Name the blood parasite species.
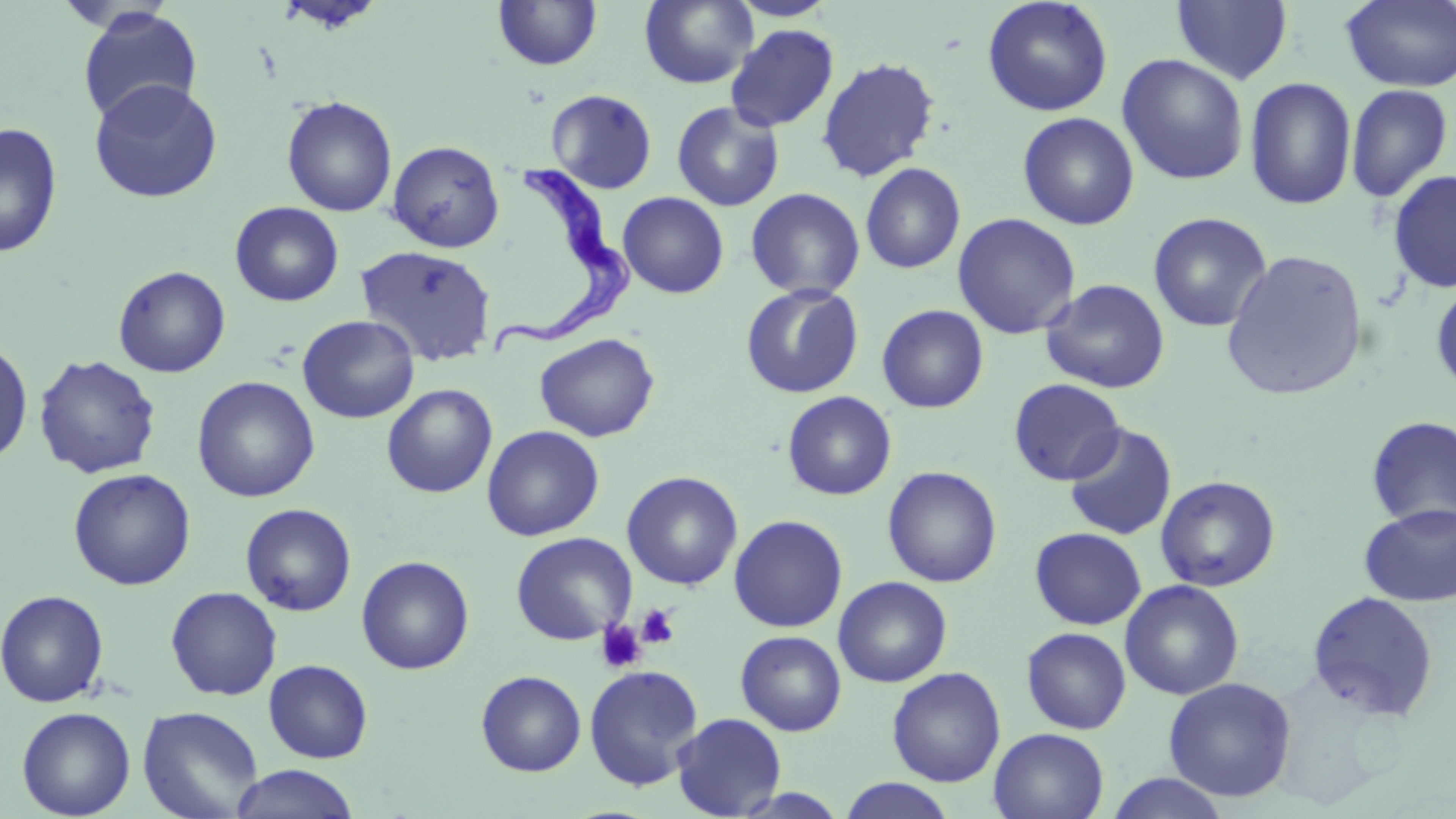

Trypanosoma brucei.

Summary:
  - Coordinate format: approximate bounding boxes as named x1/y1/x2/y2 corners in pixels
  - Uninfected red blood cell locations: (x1=274, y1=0, x2=387, y2=33), (x1=728, y1=0, x2=838, y2=22), (x1=1171, y1=0, x2=1294, y2=85), (x1=492, y1=1, x2=603, y2=71), (x1=639, y1=1, x2=758, y2=89), (x1=982, y1=1, x2=1113, y2=117), (x1=1341, y1=1, x2=1456, y2=92), (x1=77, y1=6, x2=202, y2=125), (x1=725, y1=24, x2=839, y2=132), (x1=1117, y1=53, x2=1249, y2=186), (x1=816, y1=57, x2=940, y2=182), (x1=1244, y1=76, x2=1357, y2=211), (x1=88, y1=78, x2=223, y2=203), (x1=1345, y1=83, x2=1454, y2=203), (x1=546, y1=88, x2=657, y2=194), (x1=281, y1=96, x2=397, y2=217), (x1=671, y1=101, x2=785, y2=212), (x1=1017, y1=112, x2=1139, y2=230), (x1=0, y1=122, x2=63, y2=258), (x1=387, y1=140, x2=505, y2=253), (x1=860, y1=162, x2=966, y2=274), (x1=1387, y1=169, x2=1456, y2=294), (x1=745, y1=187, x2=865, y2=301), (x1=617, y1=192, x2=729, y2=299), (x1=230, y1=201, x2=344, y2=306), (x1=1148, y1=212, x2=1272, y2=333), (x1=952, y1=213, x2=1081, y2=340), (x1=356, y1=244, x2=497, y2=366), (x1=1221, y1=248, x2=1369, y2=402), (x1=113, y1=266, x2=231, y2=378), (x1=1040, y1=278, x2=1171, y2=394), (x1=1430, y1=281, x2=1456, y2=397), (x1=740, y1=283, x2=863, y2=398), (x1=876, y1=305, x2=989, y2=413), (x1=297, y1=315, x2=420, y2=423), (x1=534, y1=333, x2=660, y2=442), (x1=0, y1=337, x2=34, y2=468), (x1=33, y1=354, x2=162, y2=479), (x1=192, y1=375, x2=320, y2=503), (x1=1008, y1=378, x2=1126, y2=486), (x1=381, y1=383, x2=498, y2=498), (x1=782, y1=391, x2=897, y2=501), (x1=1366, y1=415, x2=1456, y2=531), (x1=1063, y1=423, x2=1177, y2=540), (x1=482, y1=425, x2=604, y2=541), (x1=882, y1=466, x2=1002, y2=587), (x1=68, y1=468, x2=196, y2=590), (x1=622, y1=471, x2=742, y2=590), (x1=1155, y1=475, x2=1281, y2=592), (x1=240, y1=503, x2=356, y2=615), (x1=1359, y1=503, x2=1456, y2=606), (x1=729, y1=514, x2=848, y2=632), (x1=1029, y1=527, x2=1146, y2=630), (x1=511, y1=532, x2=636, y2=645), (x1=356, y1=555, x2=474, y2=674), (x1=833, y1=576, x2=952, y2=687), (x1=1120, y1=579, x2=1244, y2=700), (x1=165, y1=586, x2=282, y2=700), (x1=0, y1=589, x2=110, y2=708), (x1=1307, y1=590, x2=1439, y2=722), (x1=1021, y1=627, x2=1131, y2=734), (x1=736, y1=630, x2=846, y2=736), (x1=263, y1=660, x2=373, y2=763), (x1=584, y1=664, x2=703, y2=790), (x1=887, y1=666, x2=1005, y2=787), (x1=475, y1=670, x2=587, y2=776), (x1=1163, y1=677, x2=1297, y2=802), (x1=137, y1=705, x2=264, y2=819), (x1=16, y1=706, x2=136, y2=819), (x1=671, y1=712, x2=787, y2=818), (x1=989, y1=727, x2=1110, y2=819), (x1=229, y1=765, x2=361, y2=819), (x1=1105, y1=773, x2=1233, y2=819), (x1=836, y1=778, x2=958, y2=818)
  - Platelet locations: (x1=636, y1=604, x2=680, y2=649), (x1=595, y1=620, x2=646, y2=674)
  - Trypanosoma brucei locations: (x1=491, y1=157, x2=641, y2=361)
  - Image size: 1456×819 pixels
  - Magnification: 1000x
  - Preparation: thin blood film
  - Field of view: single
  - Modality: light microscopy
  - Stain: May-Grünwald-Giemsa